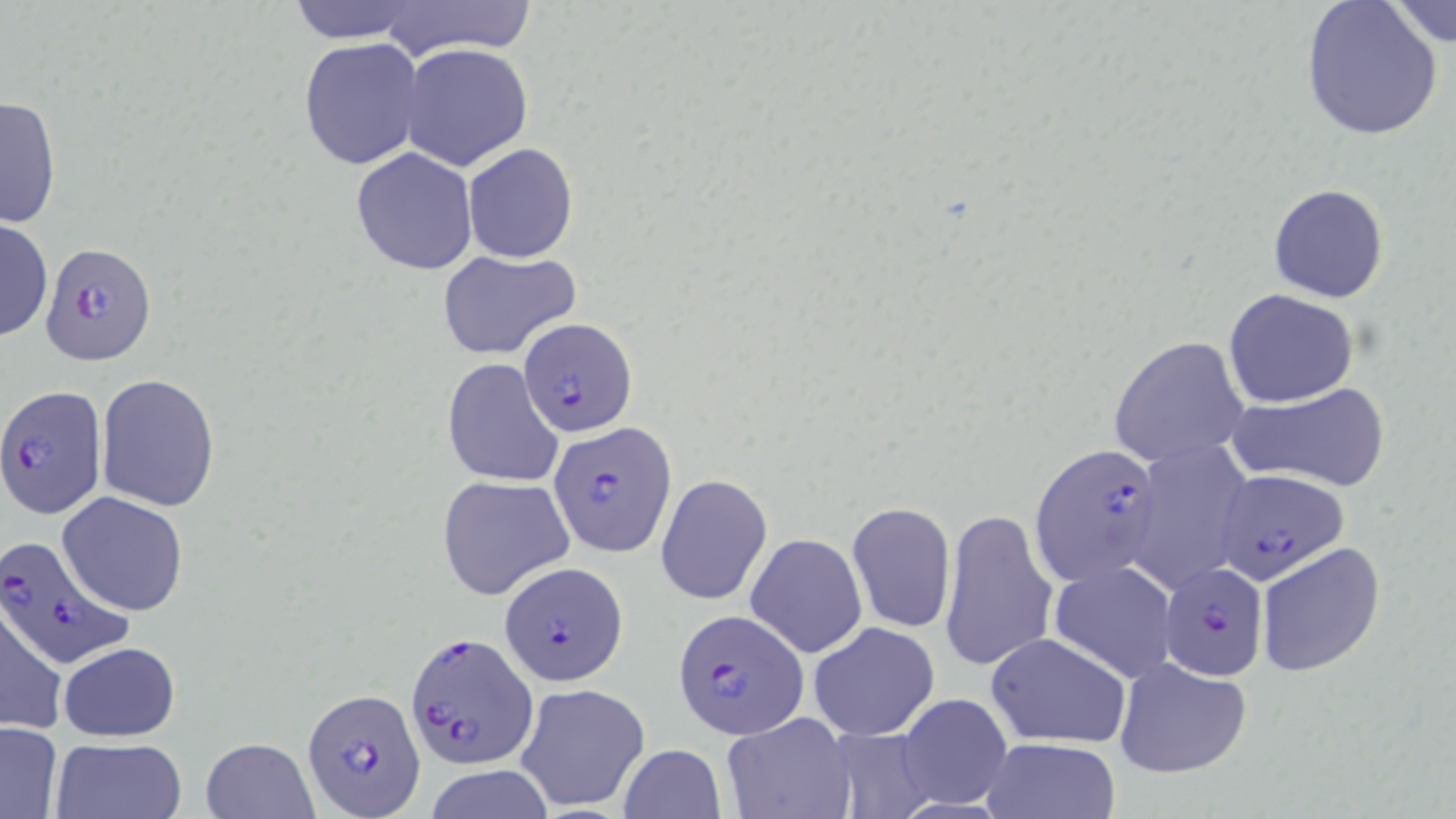 Approximate bounding boxes as named x1/y1/x2/y2 corners in pixels. Uninfected red blood cell locations: (x1=1299, y1=0, x2=1443, y2=141), (x1=281, y1=1, x2=428, y2=44), (x1=367, y1=2, x2=546, y2=60), (x1=1388, y1=3, x2=1454, y2=55), (x1=298, y1=37, x2=423, y2=171), (x1=399, y1=42, x2=534, y2=172), (x1=1, y1=94, x2=61, y2=231), (x1=462, y1=142, x2=579, y2=264), (x1=350, y1=148, x2=477, y2=275), (x1=1268, y1=182, x2=1390, y2=304), (x1=1, y1=219, x2=52, y2=341), (x1=437, y1=247, x2=583, y2=361), (x1=1224, y1=288, x2=1359, y2=407), (x1=1109, y1=336, x2=1252, y2=470), (x1=441, y1=358, x2=564, y2=489), (x1=94, y1=373, x2=221, y2=512), (x1=1221, y1=381, x2=1393, y2=493), (x1=1131, y1=438, x2=1254, y2=591), (x1=656, y1=474, x2=773, y2=605), (x1=436, y1=476, x2=575, y2=600), (x1=58, y1=491, x2=189, y2=615), (x1=846, y1=501, x2=956, y2=634), (x1=940, y1=508, x2=1058, y2=673), (x1=745, y1=532, x2=868, y2=659), (x1=1255, y1=541, x2=1386, y2=677), (x1=1050, y1=561, x2=1178, y2=683), (x1=0, y1=597, x2=66, y2=737), (x1=808, y1=621, x2=940, y2=742), (x1=986, y1=631, x2=1133, y2=749), (x1=57, y1=640, x2=181, y2=742), (x1=1114, y1=655, x2=1253, y2=780), (x1=515, y1=682, x2=652, y2=813), (x1=897, y1=694, x2=1013, y2=810), (x1=721, y1=713, x2=857, y2=819), (x1=0, y1=721, x2=64, y2=817), (x1=824, y1=726, x2=939, y2=818), (x1=979, y1=735, x2=1121, y2=819), (x1=50, y1=736, x2=186, y2=819), (x1=199, y1=736, x2=320, y2=819), (x1=616, y1=743, x2=726, y2=819), (x1=424, y1=763, x2=556, y2=819). Plasmodium falciparum-infected red blood cell locations: (x1=41, y1=242, x2=155, y2=366), (x1=518, y1=317, x2=637, y2=437), (x1=1, y1=385, x2=106, y2=519), (x1=549, y1=422, x2=676, y2=557), (x1=1031, y1=442, x2=1165, y2=588), (x1=1217, y1=470, x2=1350, y2=587), (x1=0, y1=533, x2=133, y2=669), (x1=1159, y1=560, x2=1269, y2=681), (x1=500, y1=561, x2=627, y2=683), (x1=672, y1=609, x2=808, y2=739), (x1=406, y1=632, x2=538, y2=769), (x1=303, y1=688, x2=425, y2=816). Slide-level diagnosis: Plasmodium falciparum. May-Grünwald-Giemsa stain. Single field of view. Captured at 1000x magnification. Thin blood film. Image is 1456×819 pixels. Light microscopy.